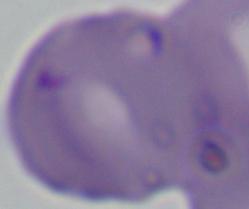
identification: Babesia
magnification: 1000x
modality: micrograph